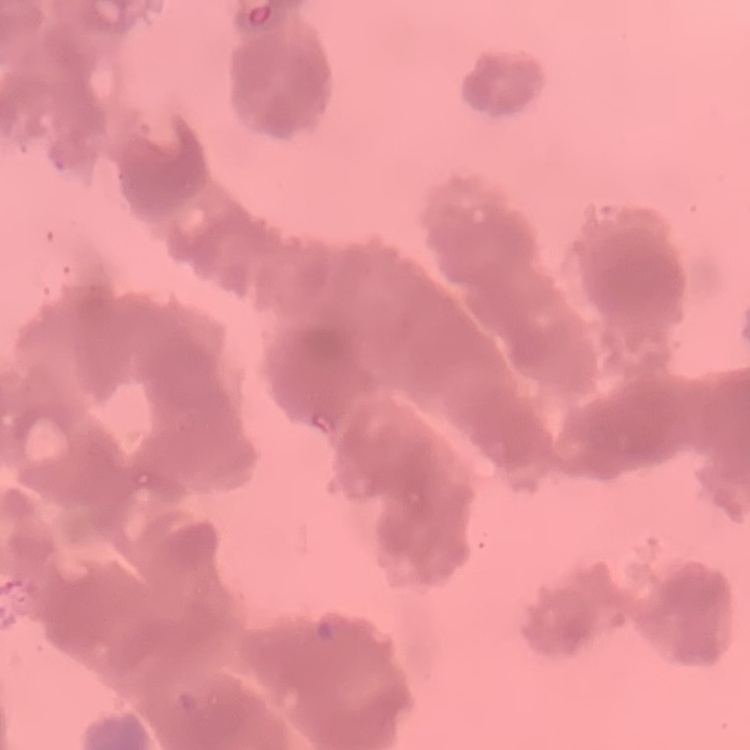
Summary:
  - Red blood cell morphology: rouleaux formation
  - Image type: one tile cut from a larger photomicrograph
  - Stain: Field's or Giemsa
  - Preparation: thin blood film